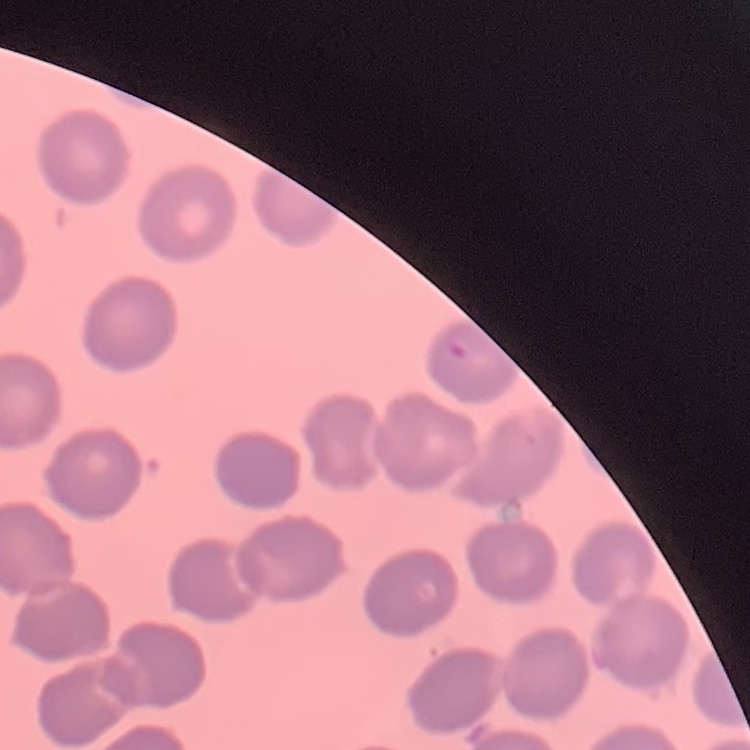

red blood cell morphology = no rouleaux formation
stain = Field's or Giemsa
preparation = thin blood film
image type = square crop of a larger photomicrograph